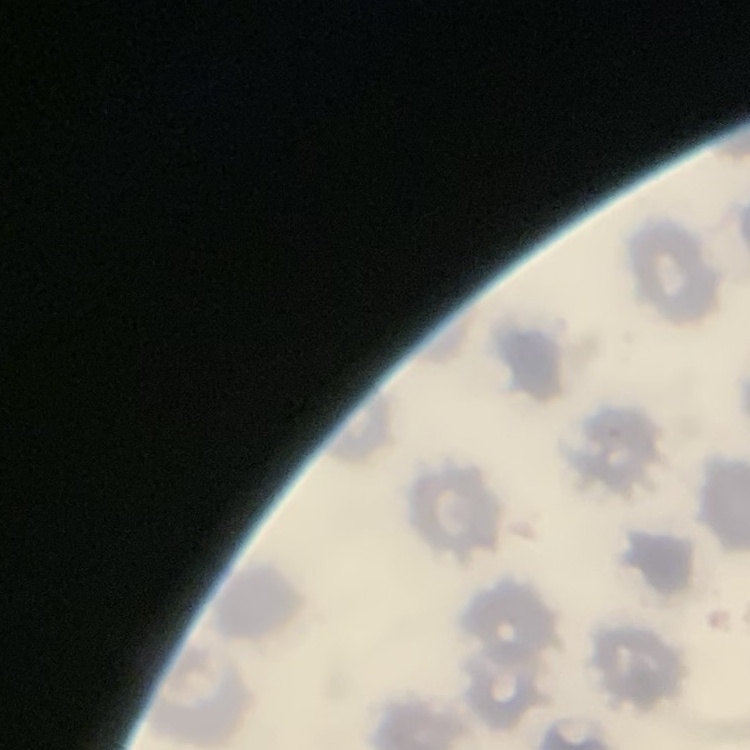 The red blood cells exhibit no rouleaux formation. Thin peripheral smear. Stained with either Field's or Giemsa. Square crop of a larger photomicrograph.